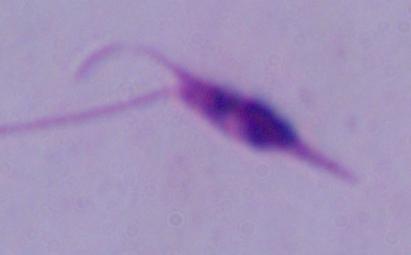
identification: Leishmania
modality: photomicrograph
magnification: 1000x